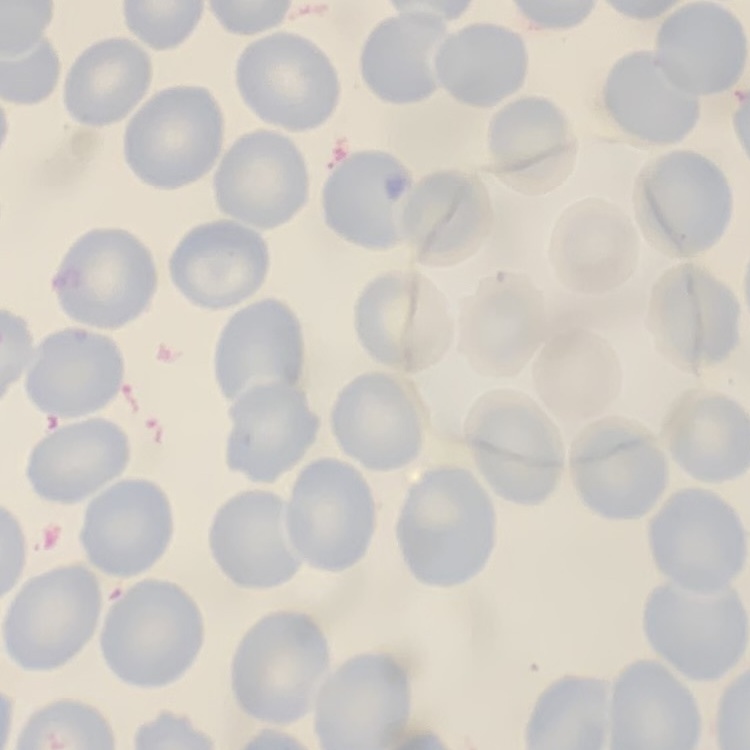 The red blood cells show no rouleaux formation. Thin blood film. One tile cut from a larger photomicrograph. Stained with either Field's or Giemsa.